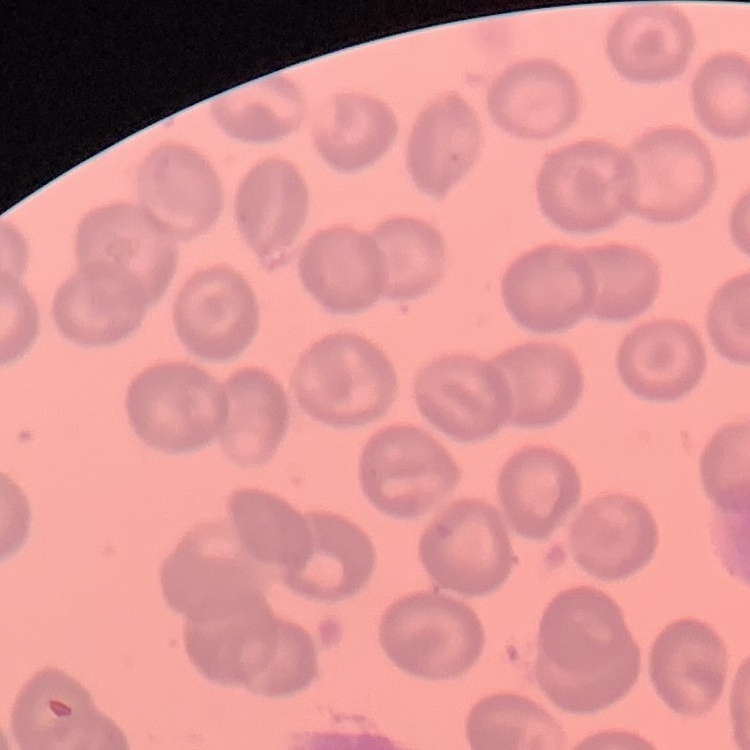

The erythrocytes show no rouleaux formation. One tile cut from a larger photomicrograph. Field's or Giemsa stain. Thin blood smear.